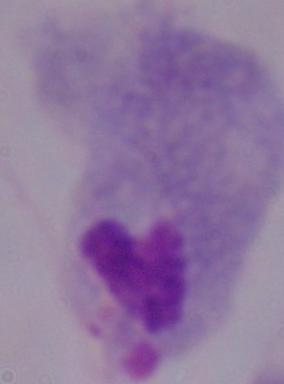

1000x magnification. A trichomonad is seen. Micrograph.